Assess this cell for malaria.
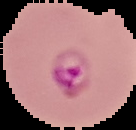

Parasitized.

preparation = thin blood film
image type = cell region segmented out of the field of view; surrounding area masked to black
image size = 136×130 pixels